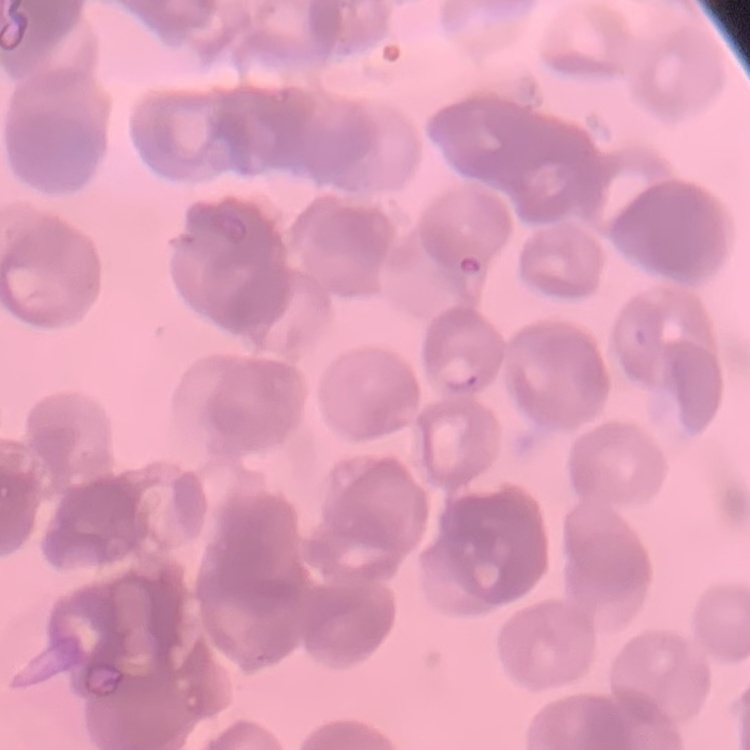
The erythrocytes show rouleaux formation. One tile cut from a larger photomicrograph. Stained with either Field's or Giemsa. Thin blood smear.